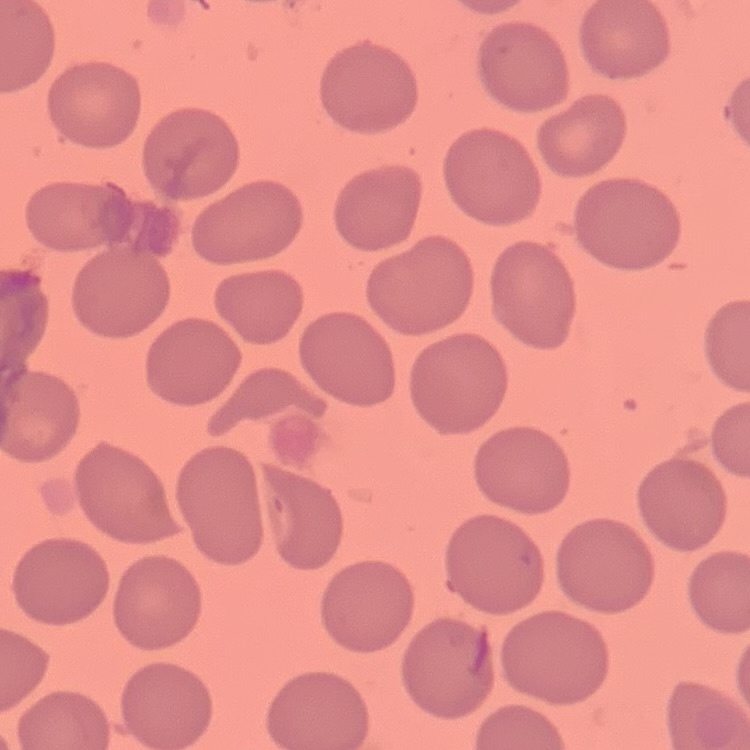 The erythrocytes show no rouleaux formation. Thin blood smear. Stained with either Field's or Giemsa. Square crop of a larger photomicrograph.